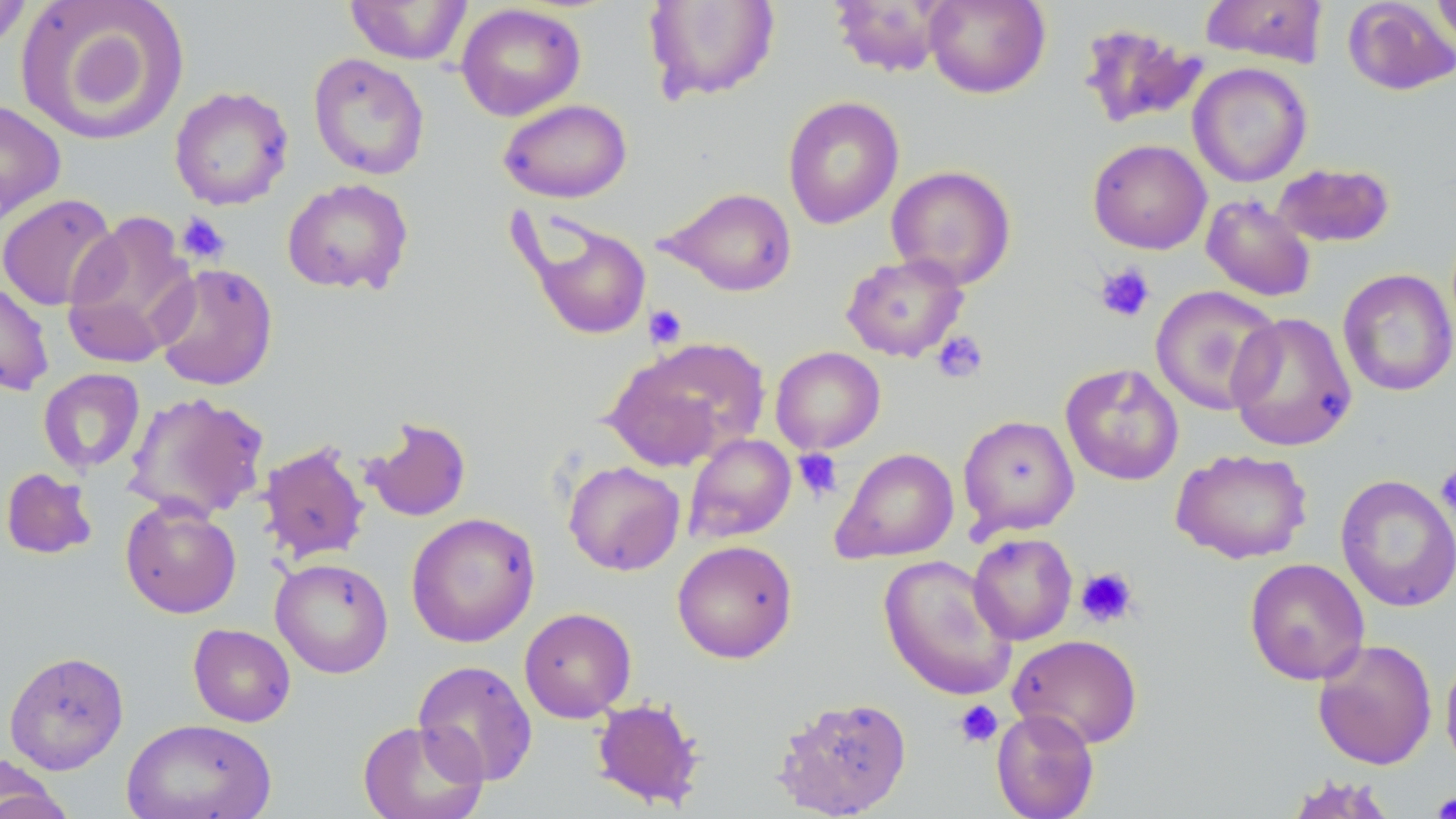 Approximate bounding boxes as named x1/y1/x2/y2 corners in pixels. Platelet locations: (x1=176, y1=213, x2=230, y2=264), (x1=1094, y1=263, x2=1155, y2=323), (x1=644, y1=304, x2=687, y2=348), (x1=931, y1=330, x2=989, y2=383), (x1=792, y1=448, x2=843, y2=501), (x1=1435, y1=463, x2=1456, y2=520), (x1=1075, y1=567, x2=1139, y2=628), (x1=953, y1=700, x2=1003, y2=749), (x1=1431, y1=789, x2=1456, y2=819). Uninfected red blood cell locations: (x1=15, y1=0, x2=191, y2=147), (x1=344, y1=0, x2=473, y2=65), (x1=828, y1=0, x2=954, y2=77), (x1=924, y1=0, x2=1051, y2=99), (x1=1199, y1=0, x2=1329, y2=67), (x1=1431, y1=0, x2=1456, y2=58), (x1=0, y1=1, x2=34, y2=54), (x1=643, y1=1, x2=781, y2=103), (x1=1342, y1=1, x2=1456, y2=96), (x1=455, y1=3, x2=586, y2=121), (x1=1078, y1=23, x2=1208, y2=130), (x1=308, y1=52, x2=430, y2=180), (x1=1188, y1=63, x2=1312, y2=187), (x1=169, y1=85, x2=294, y2=210), (x1=782, y1=96, x2=905, y2=229), (x1=0, y1=98, x2=66, y2=227), (x1=498, y1=99, x2=632, y2=203), (x1=1087, y1=139, x2=1211, y2=254), (x1=1271, y1=162, x2=1395, y2=248), (x1=886, y1=165, x2=1017, y2=289), (x1=281, y1=177, x2=414, y2=295), (x1=660, y1=186, x2=797, y2=297), (x1=0, y1=193, x2=120, y2=311), (x1=1201, y1=194, x2=1316, y2=302), (x1=62, y1=209, x2=199, y2=369), (x1=517, y1=211, x2=654, y2=342), (x1=840, y1=252, x2=969, y2=363), (x1=151, y1=262, x2=278, y2=391), (x1=1338, y1=268, x2=1456, y2=397), (x1=0, y1=279, x2=54, y2=396), (x1=1150, y1=285, x2=1283, y2=416), (x1=1226, y1=311, x2=1357, y2=452), (x1=604, y1=338, x2=768, y2=470), (x1=770, y1=346, x2=885, y2=454), (x1=1060, y1=363, x2=1184, y2=486), (x1=38, y1=368, x2=145, y2=474), (x1=123, y1=391, x2=269, y2=523), (x1=957, y1=415, x2=1079, y2=538), (x1=363, y1=416, x2=473, y2=522), (x1=683, y1=434, x2=796, y2=543), (x1=258, y1=440, x2=370, y2=565), (x1=832, y1=447, x2=959, y2=563), (x1=1171, y1=448, x2=1313, y2=565), (x1=563, y1=460, x2=685, y2=576), (x1=1, y1=467, x2=98, y2=560), (x1=1335, y1=474, x2=1456, y2=612), (x1=120, y1=498, x2=242, y2=618), (x1=405, y1=512, x2=540, y2=648), (x1=968, y1=533, x2=1077, y2=645), (x1=671, y1=540, x2=798, y2=663), (x1=878, y1=555, x2=1017, y2=700), (x1=1244, y1=557, x2=1370, y2=685), (x1=271, y1=558, x2=394, y2=678), (x1=519, y1=607, x2=637, y2=723), (x1=188, y1=624, x2=296, y2=727), (x1=1008, y1=633, x2=1143, y2=749), (x1=1312, y1=638, x2=1437, y2=770), (x1=1441, y1=649, x2=1456, y2=774), (x1=3, y1=650, x2=130, y2=774), (x1=413, y1=659, x2=539, y2=786), (x1=773, y1=695, x2=913, y2=818), (x1=590, y1=697, x2=706, y2=810), (x1=990, y1=709, x2=1100, y2=819), (x1=121, y1=717, x2=277, y2=819), (x1=357, y1=719, x2=488, y2=819), (x1=0, y1=757, x2=73, y2=818), (x1=1283, y1=774, x2=1402, y2=818). Slide-level diagnosis: no evidence of blood parasites. Image is 1456×819 pixels. One field of a larger specimen. May-Grünwald-Giemsa stain. Thin blood smear. Optical microscopy. Captured at 1000x magnification.